Classify this cell by malaria status.
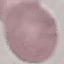
Uninfected.

Cell patch, automatically extracted from a larger field of view and resized to 64 × 64 pixels. Giemsa stain. Acquired by smartphone through the microscope eyepiece. Thin smear of blood.